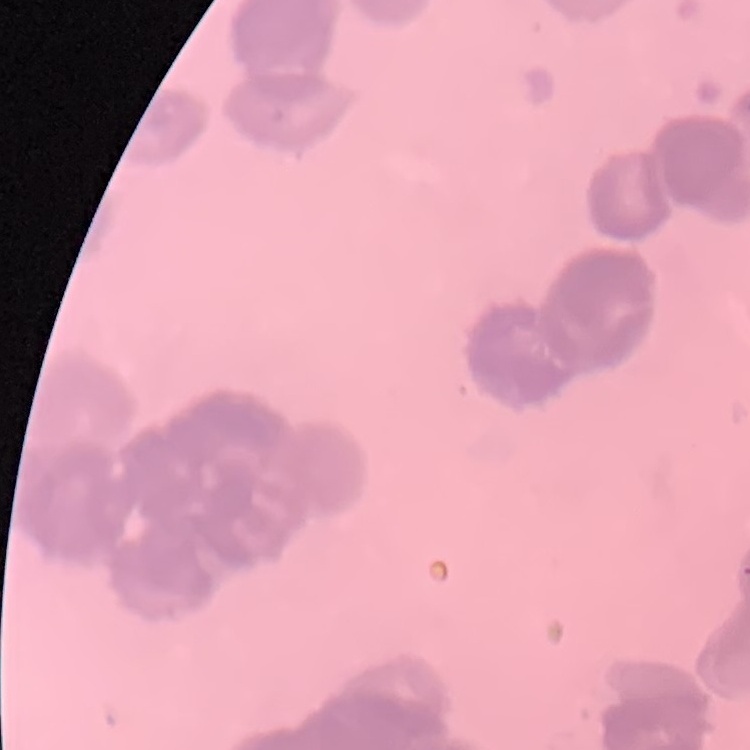

red_blood_cell_morphology: rouleaux formation
preparation: thin blood film
stain: Field's or Giemsa
image_type: square crop of a larger photomicrograph